Name the blood parasite species.
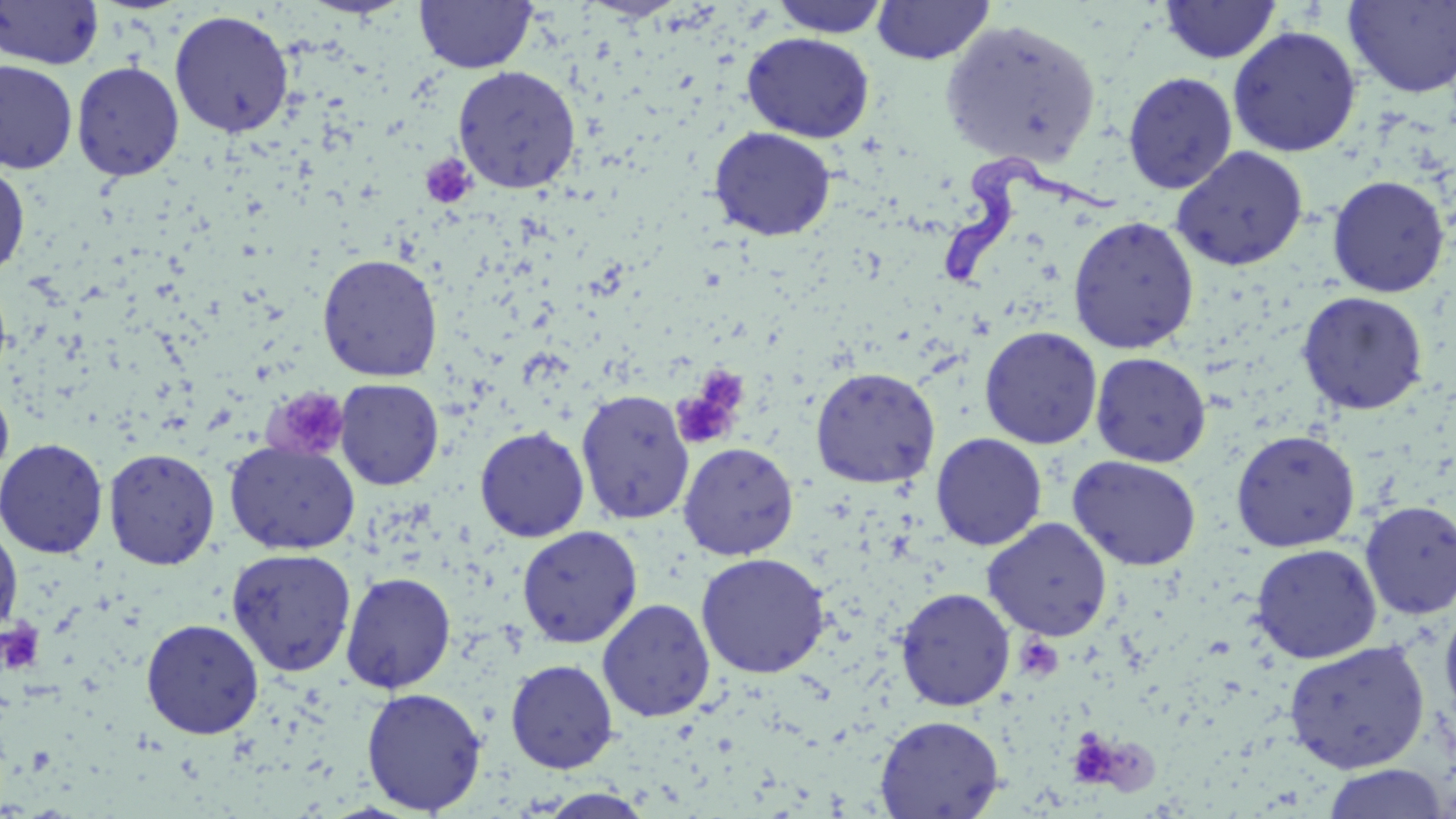

Trypanosoma brucei.

Approximate bounding boxes as (x1,y1)-(x2,y2) corner pairs in pixels. Trypanosoma brucei locations: (942,152)-(1121,287). Uninfected red blood cell locations: (0,0)-(104,69), (414,0)-(538,74), (581,0)-(687,20), (768,0)-(893,38), (871,0)-(995,65), (1159,1)-(1281,64), (1344,1)-(1456,99), (169,9)-(295,139), (940,18)-(1102,168), (1227,25)-(1362,157), (742,32)-(875,143), (0,60)-(78,174), (71,61)-(184,181), (452,65)-(582,193), (1122,71)-(1238,194), (708,126)-(836,242), (1171,146)-(1308,271), (0,164)-(30,280), (1327,175)-(1451,297), (1067,215)-(1200,354), (317,254)-(443,382), (1296,290)-(1429,416), (979,325)-(1103,450), (1090,352)-(1211,467), (810,366)-(941,489), (334,378)-(444,490), (0,383)-(14,485), (575,389)-(696,525), (474,426)-(590,542), (1230,429)-(1361,551), (930,433)-(1048,551), (0,438)-(109,559), (224,440)-(360,555), (677,442)-(799,560), (104,447)-(220,570), (1067,455)-(1202,571), (1359,500)-(1456,619), (982,518)-(1113,641), (0,523)-(23,633), (516,525)-(642,648), (1250,543)-(1382,663), (226,548)-(357,677), (695,552)-(831,678), (341,571)-(456,694), (895,587)-(1015,711), (597,597)-(716,722), (1439,601)-(1456,733), (140,618)-(265,739), (1283,640)-(1430,774), (505,658)-(618,774), (361,686)-(487,813), (875,714)-(1004,818), (1320,764)-(1450,818), (537,789)-(656,819). Platelet locations: (420,154)-(476,209), (672,370)-(748,449), (267,388)-(350,461), (1,620)-(45,675), (1015,636)-(1064,681), (1077,737)-(1112,784). Single field of view. Image is 1456×819 pixels. Light microscopy. 1000x magnification. May-Grünwald-Giemsa stain. Thin blood film.